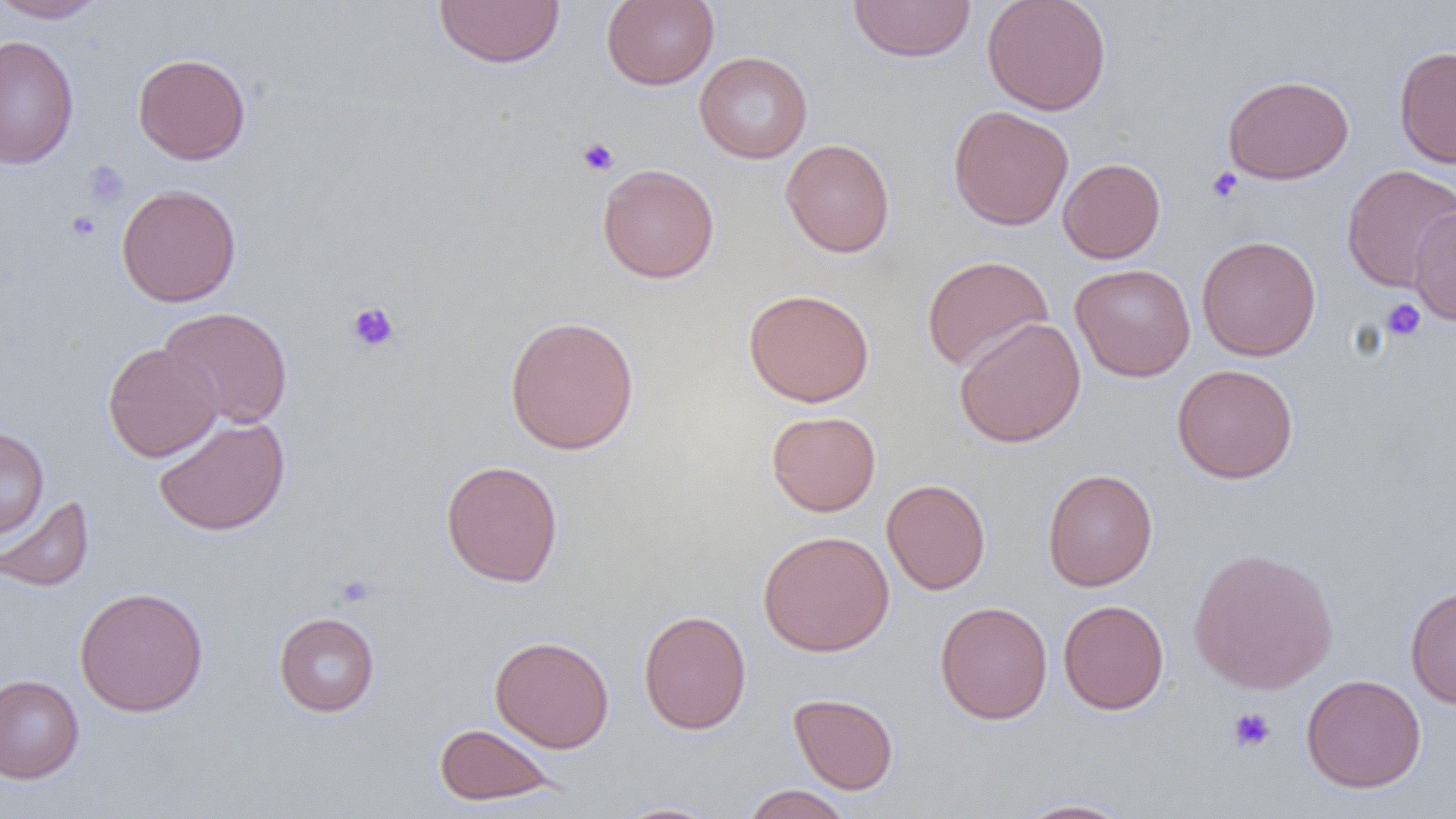
slide_level_diagnosis: negative for blood parasites
modality: light microscopy
uninfected_red_blood_cell_locations: 'approximate bounding boxes as [x1, y1, x2, y2] in pixels: [0, 0, 109, 23], [432, 0, 565, 69], [601, 0, 719, 90], [981, 0, 1112, 116], [848, 1, 976, 63], [0, 35, 79, 170], [1393, 45, 1456, 168], [694, 51, 813, 163], [132, 52, 251, 165], [1222, 74, 1354, 184], [948, 105, 1074, 230], [780, 138, 895, 258], [1058, 158, 1166, 264], [597, 163, 720, 284], [1341, 164, 1456, 292], [116, 183, 242, 307], [1408, 204, 1456, 326], [1196, 235, 1321, 361], [921, 255, 1053, 373], [1069, 263, 1196, 382], [743, 287, 875, 407], [158, 306, 293, 429], [503, 315, 640, 455], [954, 316, 1086, 448], [103, 342, 222, 462], [1171, 364, 1298, 483], [766, 411, 881, 516], [153, 414, 291, 536], [0, 426, 49, 538], [440, 459, 564, 587], [1042, 468, 1158, 591], [881, 478, 991, 595], [0, 494, 95, 592], [757, 529, 894, 656], [1187, 547, 1339, 695], [1405, 585, 1456, 709], [74, 586, 209, 717], [1058, 599, 1169, 714], [934, 601, 1053, 724], [638, 609, 751, 735], [273, 611, 380, 717], [489, 635, 615, 753], [1300, 673, 1426, 793], [0, 674, 84, 783], [788, 692, 899, 794], [434, 722, 559, 806], [741, 784, 854, 819], [1013, 797, 1138, 818], [609, 801, 725, 818]'
image_size: 1456×819 pixels
field_of_view: single
platelet_locations: 'approximate bounding boxes as [x1, y1, x2, y2] in pixels: [576, 138, 619, 176], [83, 159, 130, 209], [1206, 167, 1242, 203], [66, 210, 100, 241], [1381, 298, 1426, 341], [346, 301, 401, 352], [334, 574, 376, 607], [1227, 706, 1276, 753]'
magnification: 1000x
preparation: thin blood film